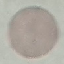

Result: no malaria parasites detected. Giemsa-stained preparation. Thin smear of blood. Photographed with a smartphone camera at the microscope eyepiece. Automatically extracted cell patch, resized to 64 × 64 pixels.